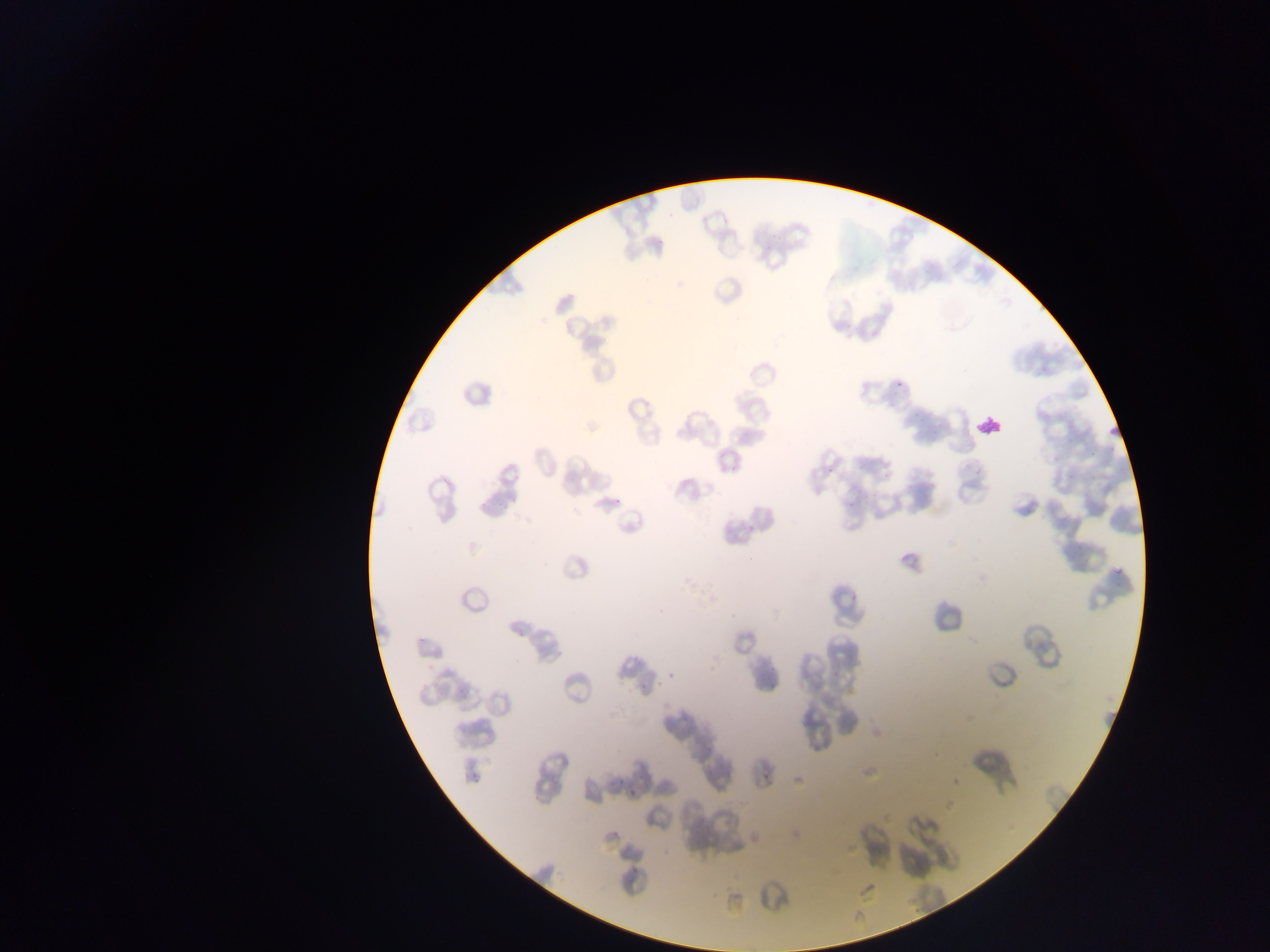 Approximate bounding boxes as [left, top, right, bottom] in pixels. Leukocyte locations: [971, 410, 1008, 444]. Plasmodium parasite locations: [1103, 424, 1121, 438], [1110, 561, 1124, 579]. Collected in Ghana. Photographed through a microscope with a mobile-phone camera. Thin blood smear. Single field of view. Image is 1270×952 pixels.